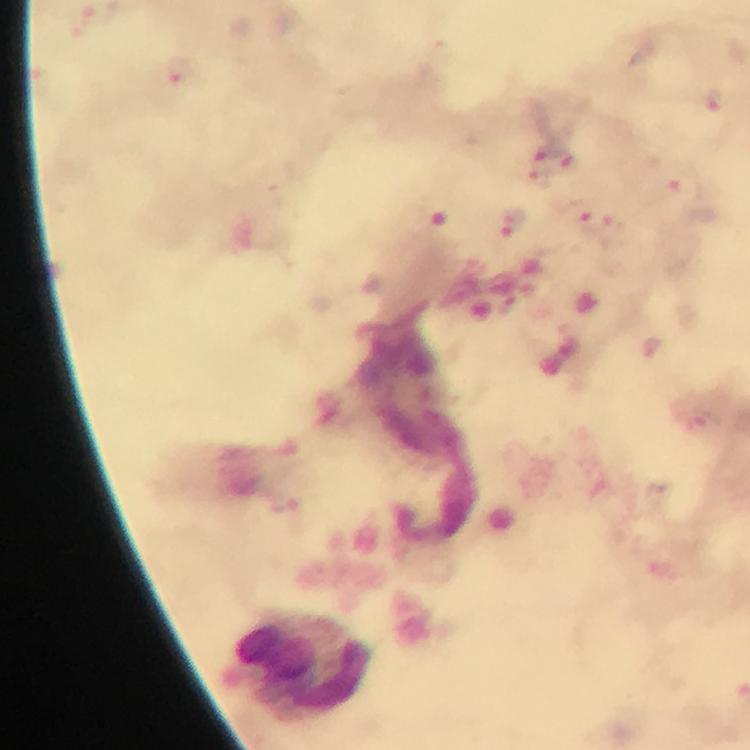

Approximate object centers, in pixels from the top-left corner. Leukocyte locations: (x=302, y=667). Malaria parasite locations: (x=179, y=71), (x=713, y=102), (x=545, y=154), (x=566, y=159), (x=539, y=176), (x=680, y=181), (x=597, y=222), (x=510, y=224), (x=651, y=347). Immersion oil was used. Cropped region of a single field of view. 100x magnification. Photographed through the microscope with a smartphone camera. Image is 750×750 pixels. Thick smear. From a diagnostic examination for malaria. Giemsa stain.